Describe the morphology of the red blood cells.
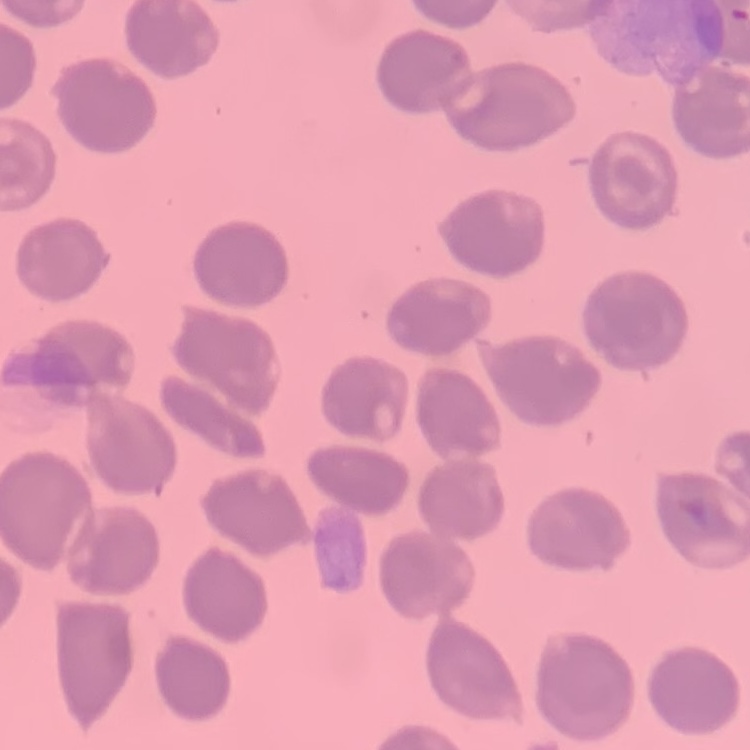

No rouleaux formation.

Field's or Giemsa stain. One tile cut from a larger photomicrograph. Thin blood film.